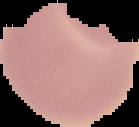

image_size: 139×127 pixels
malaria_status: uninfected
preparation: thin blood film
image_type: segmented cell region with the area outside set to black